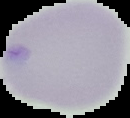
Summary:
  - Image size: 130×118 pixels
  - Preparation: thin blood film
  - Malaria status: uninfected
  - Image type: segmented cell region with the area outside set to black